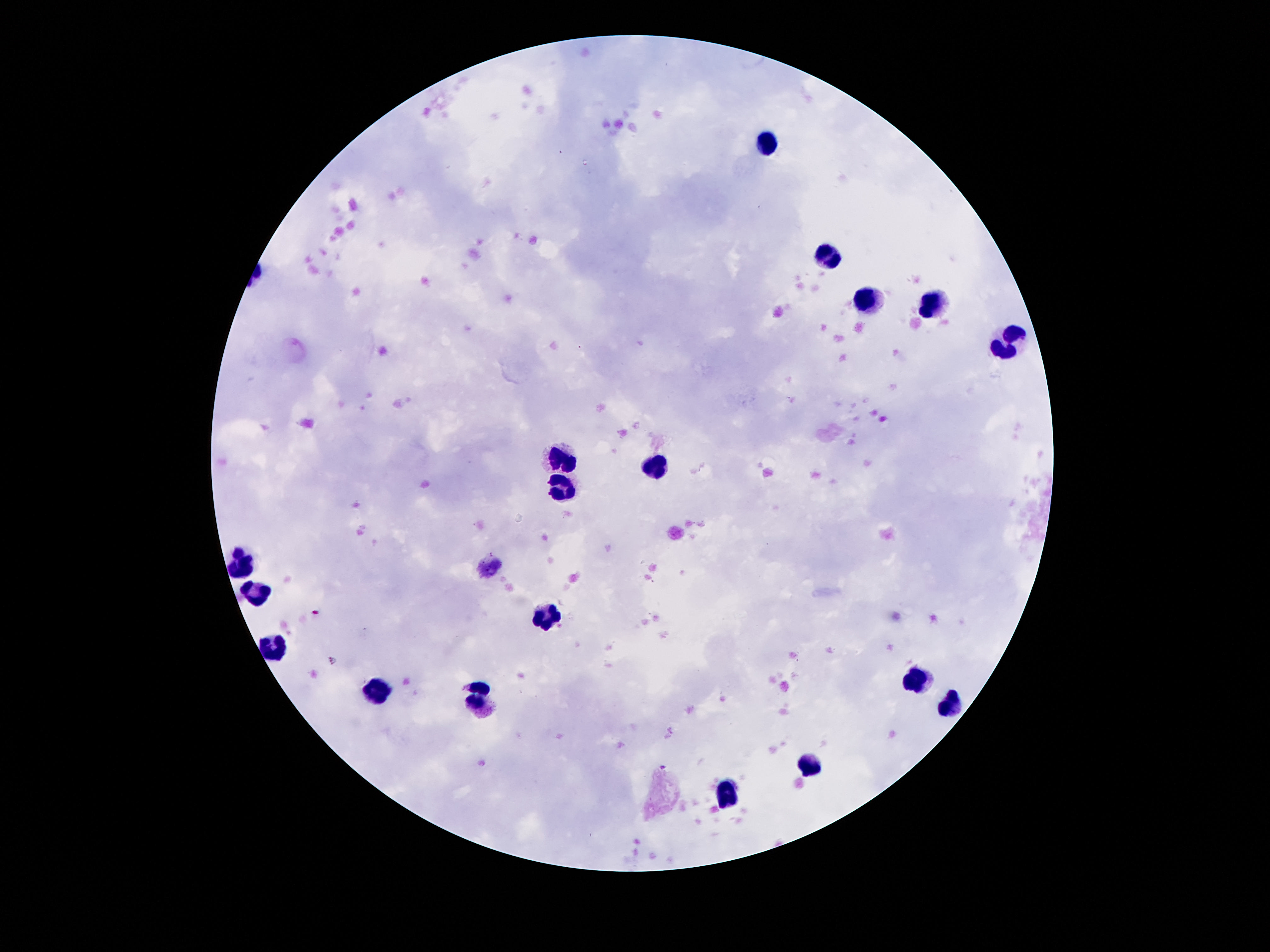

{
  "leukocyte_locations": "approximate centers as [x, y] in pixels: [769, 143], [828, 258], [870, 299], [930, 307], [1010, 338], [561, 462], [654, 466], [561, 491], [240, 568], [256, 593], [543, 617], [276, 647], [919, 680], [379, 691], [481, 696], [950, 704], [808, 765], [727, 797]",
  "capture": "smartphone camera through the microscope eyepiece",
  "patient_malaria_status": "negative",
  "preparation": "thick blood film",
  "field_of_view": "single",
  "magnification": "100x",
  "stain": "Giemsa",
  "image_size": "1270×952 pixels"
}